Assess this cell for malaria.
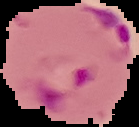
It is parasitized.

Summary:
  - Preparation: thin blood smear
  - Image type: cell region segmented out of the field of view; surrounding area masked to black
  - Image size: 139×127 pixels